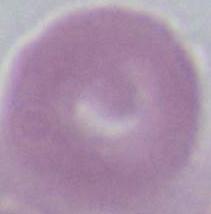

identification = red blood cell
magnification = 1000x
modality = photomicrograph